Assess this cell for malaria.
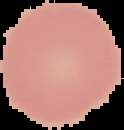
It is uninfected.

Cell region segmented out of the field of view; the surrounding area is masked to black. From a thin blood film. Image is 124×130 pixels.